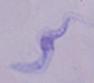
modality = photomicrograph
identification = trypanosome
magnification = 1000x